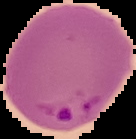

preparation = thin blood film
image size = 136×139 pixels
image type = cell region segmented out of the field of view; surrounding area masked to black
result = Plasmodium parasites detected